Identify the blood parasite species.
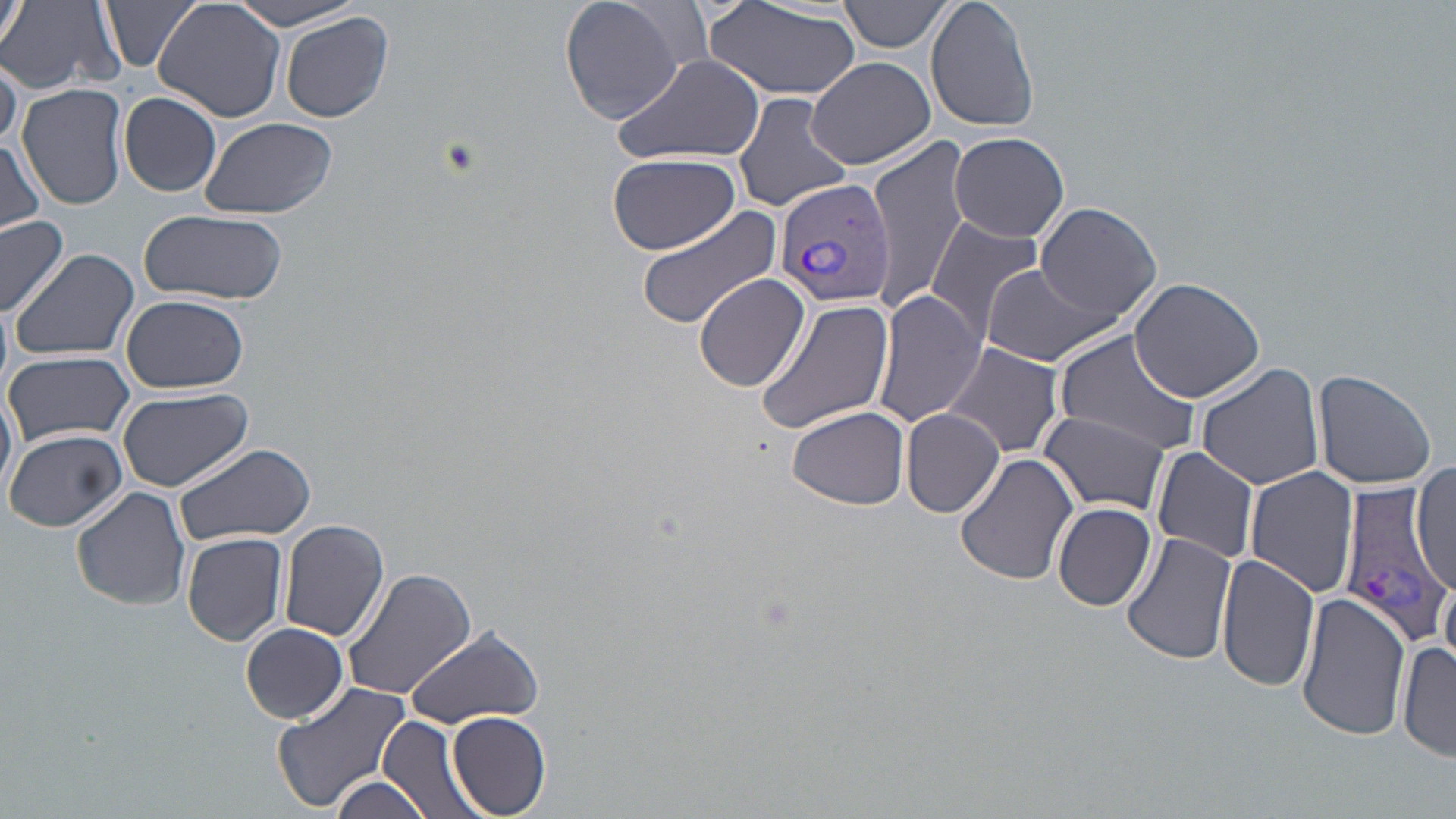
Plasmodium vivax.

Summary:
  - Coordinate format: approximate bounding boxes as (x1, y1, x2, y2) in pixels
  - Plasmodium vivax-infected red blood cell locations: (772, 176, 895, 310), (1337, 482, 1448, 645)
  - Uninfected red blood cell locations: (2, 0, 29, 54), (101, 0, 203, 73), (558, 0, 696, 123), (839, 0, 954, 54), (924, 0, 1042, 133), (0, 1, 124, 96), (155, 1, 287, 121), (226, 1, 370, 32), (701, 1, 862, 100), (279, 11, 395, 126), (0, 50, 21, 154), (612, 52, 765, 166), (805, 55, 935, 170), (755, 69, 901, 190), (19, 82, 128, 210), (118, 91, 223, 197), (733, 92, 851, 213), (199, 116, 336, 217), (948, 131, 1070, 242), (2, 136, 44, 235), (864, 136, 976, 310), (607, 152, 741, 256), (1035, 202, 1162, 320), (637, 204, 786, 328), (138, 208, 287, 306), (925, 214, 1048, 344), (0, 216, 70, 320), (8, 247, 139, 361), (980, 262, 1127, 366), (693, 271, 811, 393), (1127, 277, 1264, 402), (873, 288, 986, 428), (121, 295, 250, 394), (756, 297, 896, 435), (1053, 331, 1202, 459), (941, 340, 1065, 459), (4, 349, 134, 447), (1196, 362, 1322, 490), (1312, 367, 1436, 489), (0, 381, 17, 501), (117, 386, 253, 491), (788, 406, 911, 509), (901, 407, 1005, 519), (1038, 411, 1170, 517), (1, 427, 128, 531), (173, 441, 315, 546), (1151, 446, 1262, 564), (955, 450, 1079, 586), (1412, 460, 1455, 597), (1244, 466, 1360, 597), (72, 488, 192, 610), (1053, 501, 1157, 610), (278, 517, 391, 643), (1119, 531, 1236, 668), (182, 532, 288, 646), (1215, 554, 1320, 692), (341, 564, 477, 703), (1438, 571, 1455, 668), (1296, 592, 1411, 742), (403, 623, 546, 729), (241, 624, 350, 724), (1399, 638, 1456, 763), (272, 684, 413, 812), (447, 711, 553, 817), (379, 714, 485, 819), (326, 773, 435, 819)
  - Field of view: one of a larger specimen
  - Magnification: 1000x
  - Image size: 1456×819 pixels
  - Modality: optical microscopy
  - Stain: May-Grünwald-Giemsa
  - Preparation: thin blood film